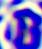

{
  "modality": "micrograph",
  "magnification": "400x",
  "identification": "white blood cell"
}